Classify this cell by malaria status.
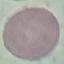

Uninfected.

Thin smear of blood. Photographed with a smartphone camera at the microscope eyepiece. Cell patch, automatically extracted from a larger field of view and resized to 64 × 64 pixels. Giemsa stain.